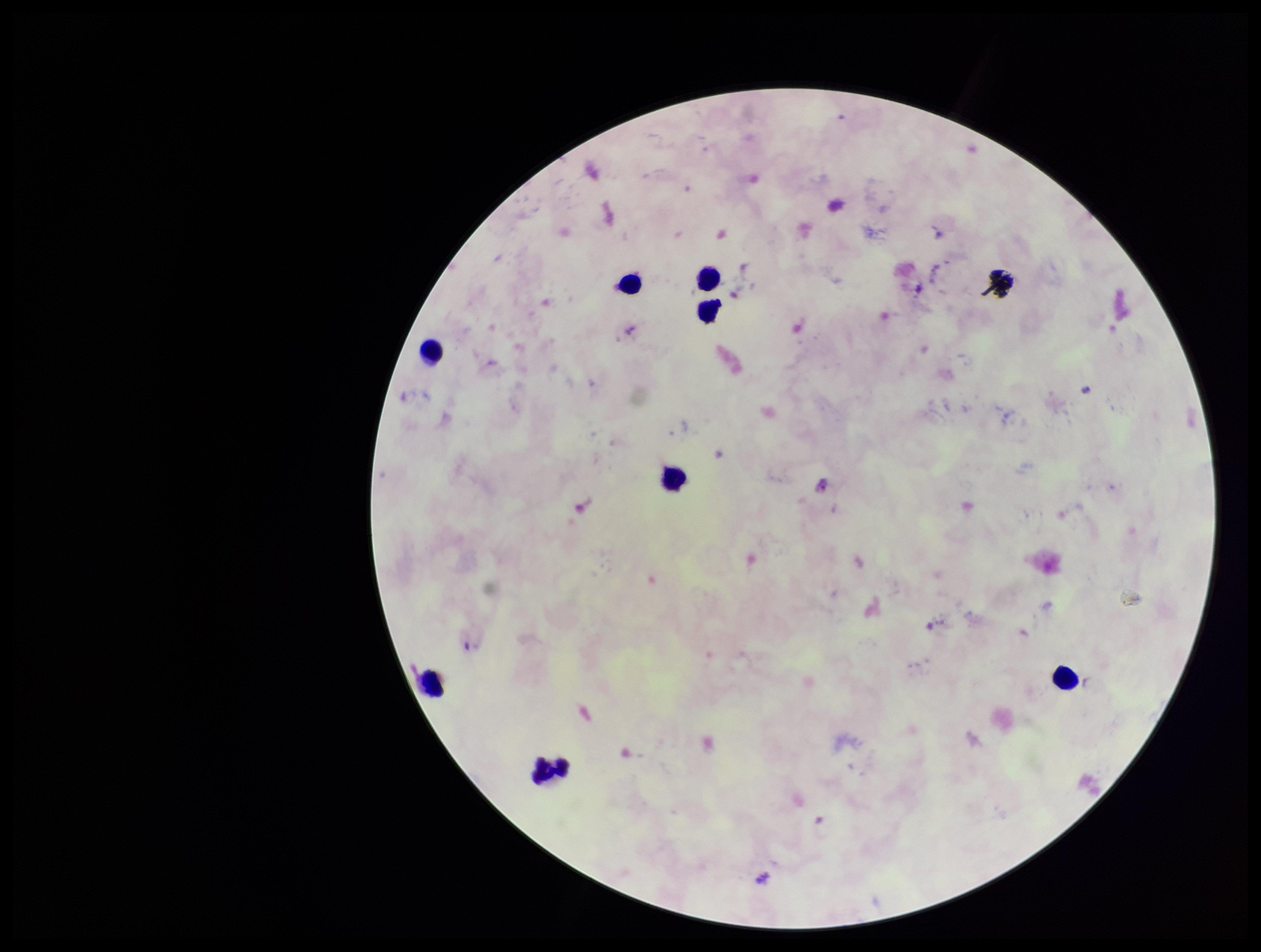
Smartphone photograph taken through the eyepiece of a microscope. Preparation: thick blood smear. Giemsa stain. One field from this slide. Leukocyte count: 8. Parasite count: 1. Species reported for this patient: Plasmodium falciparum. Patient malaria status: positive. Image is 1261×952 pixels. Plasmodium parasites: detected.